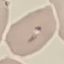
malaria status = parasitized
capture = smartphone through the microscope eyepiece
preparation = thin smear
stain = Giemsa
image type = automatically extracted cell patch, resized to 64 × 64 pixels